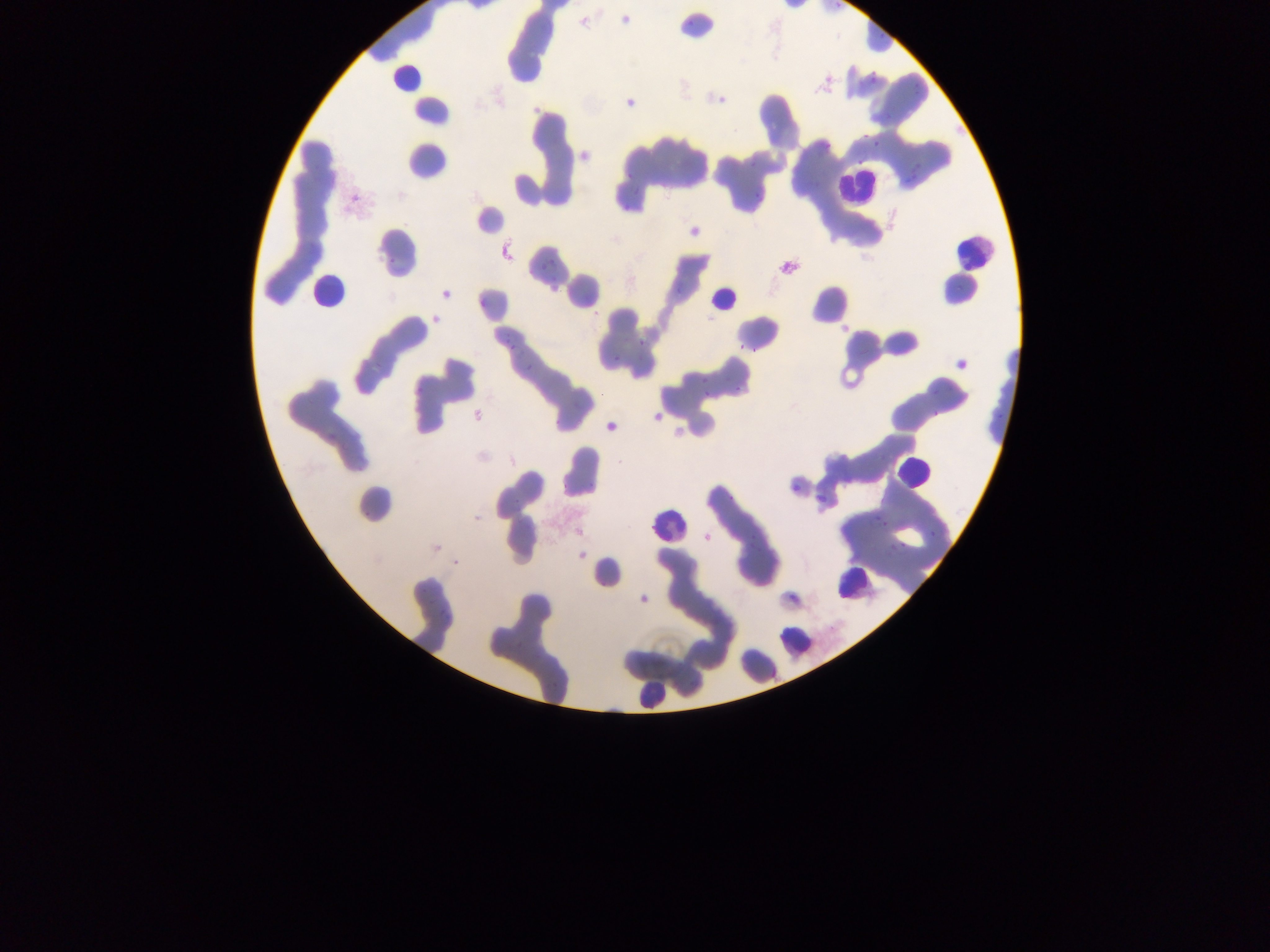
Approximate bounding boxes as (left, top, right, bottom) in pixels.
Summary:
  - Leukocyte locations: (386, 70, 423, 101), (831, 172, 874, 207), (941, 229, 988, 274), (307, 266, 344, 320), (708, 290, 737, 314), (891, 461, 926, 489), (646, 514, 686, 545), (832, 571, 868, 606), (774, 621, 806, 663), (633, 677, 671, 713)
  - Plasmodium parasite locations: (866, 77, 879, 88), (867, 136, 883, 150), (544, 255, 557, 269), (633, 334, 645, 352), (505, 337, 515, 348), (731, 337, 748, 354), (520, 350, 544, 372), (700, 375, 709, 383), (729, 385, 742, 394), (702, 396, 710, 404), (786, 481, 803, 497), (814, 497, 824, 513), (869, 510, 883, 523), (926, 528, 942, 541), (889, 538, 906, 547)
  - Image size: 1270×952 pixels
  - Capture: mobile-phone photograph through a microscope
  - Preparation: thin blood smear
  - Country: Ghana
  - Field of view: single